Comment on the morphology of the erythrocytes.
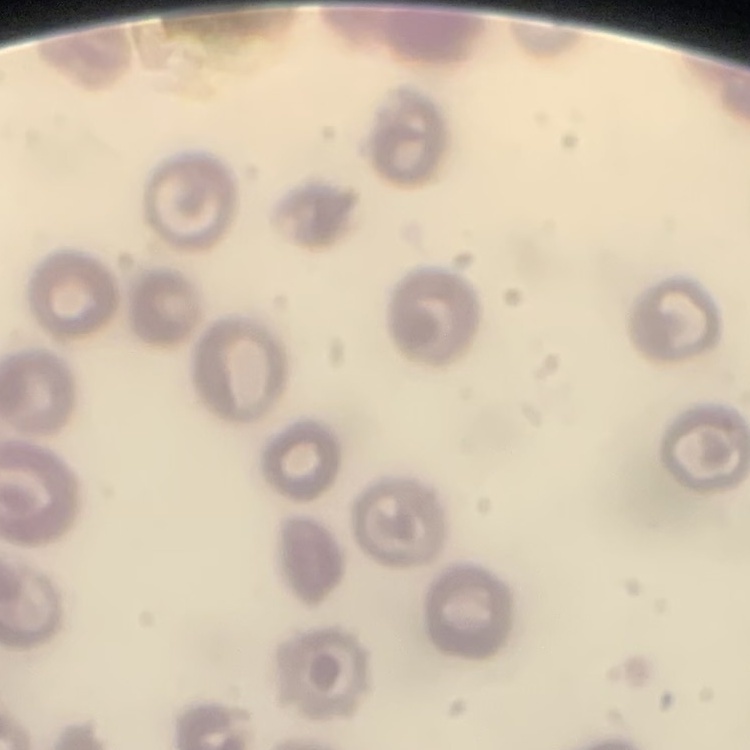
They show no rouleaux formation.

stain = Field's or Giemsa
preparation = thin blood smear
image type = one tile cut from a larger photomicrograph